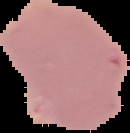
preparation = thin blood smear
malaria status = uninfected
image size = 130×133 pixels
image type = cell region segmented out of the field of view; surrounding area masked to black